Name the parasite shown.
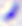

This is Toxoplasma gondii.

magnification = 400x
modality = micrograph